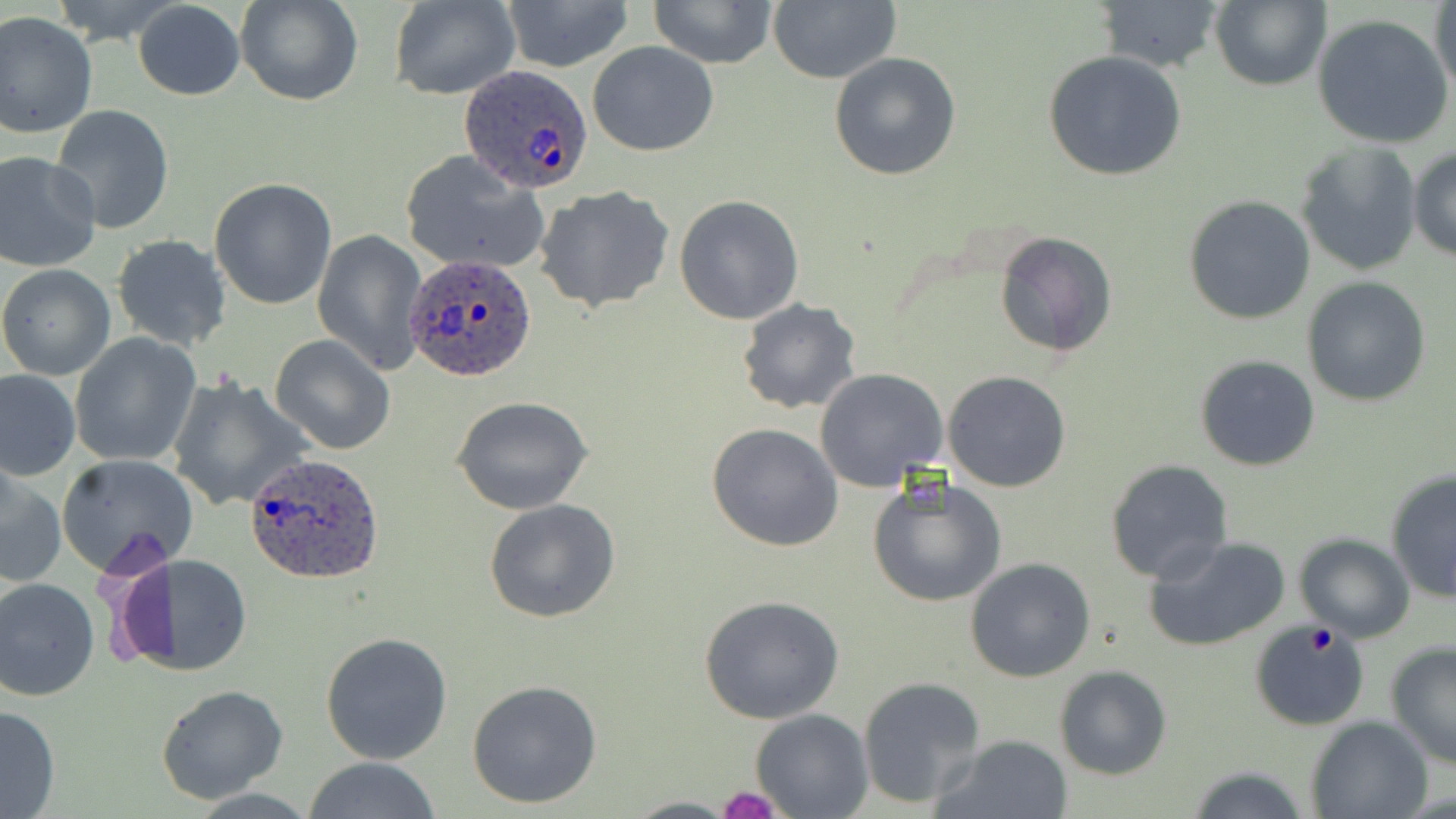

Summary:
  - Coordinate format: approximate bounding boxes as (x1, y1, x2, y2) in pixels
  - Platelet locations: (1302, 623, 1341, 658), (718, 787, 780, 819)
  - Plasmodium ovale-infected red blood cell locations: (459, 65, 593, 193), (404, 253, 540, 383), (244, 453, 389, 585)
  - Uninfected red blood cell locations: (51, 0, 185, 47), (238, 0, 362, 106), (391, 0, 521, 99), (648, 0, 779, 68), (1091, 0, 1227, 73), (1208, 0, 1331, 92), (1430, 0, 1456, 98), (132, 1, 246, 101), (501, 1, 633, 74), (767, 1, 900, 85), (0, 13, 98, 138), (1312, 15, 1454, 149), (587, 41, 719, 158), (1042, 50, 1188, 181), (829, 52, 961, 180), (50, 105, 175, 234), (1296, 142, 1421, 276), (1409, 145, 1456, 262), (400, 149, 550, 276), (0, 150, 102, 273), (209, 178, 337, 310), (536, 185, 676, 314), (674, 195, 805, 324), (1185, 195, 1316, 324), (312, 228, 430, 374), (994, 232, 1117, 358), (111, 234, 231, 352), (0, 264, 116, 380), (1302, 276, 1431, 406), (736, 298, 861, 416), (69, 332, 201, 467), (269, 335, 396, 456), (1194, 354, 1321, 471), (1, 369, 79, 479), (815, 369, 949, 493), (942, 371, 1071, 492), (169, 376, 313, 513), (453, 396, 594, 515), (706, 423, 844, 552), (57, 453, 197, 573), (1104, 459, 1235, 584), (1, 467, 67, 589), (1385, 468, 1456, 604), (867, 479, 1008, 609), (484, 498, 621, 624), (1294, 533, 1415, 640), (1142, 534, 1291, 652), (116, 554, 252, 677), (964, 558, 1095, 682), (0, 576, 100, 702), (700, 595, 844, 724), (1248, 622, 1370, 731), (320, 630, 453, 765), (1385, 642, 1456, 770), (1054, 665, 1173, 780), (858, 676, 985, 807), (466, 679, 601, 809), (155, 684, 289, 803), (0, 702, 62, 817), (752, 707, 872, 817), (1307, 715, 1432, 819), (935, 733, 1073, 818), (303, 757, 443, 818), (1185, 764, 1314, 819), (623, 797, 738, 818)
  - Slide-level diagnosis: Plasmodium ovale
  - Magnification: 1000x
  - Modality: light microscopy
  - Image size: 1456×819 pixels
  - Stain: May-Grünwald-Giemsa
  - Preparation: thin blood film
  - Field of view: one of a larger specimen